Classify this cell by malaria status.
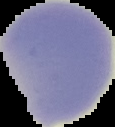

It is uninfected.

From a thin blood film. The area outside the segmented cell region is set to black. Image is 115×127 pixels.